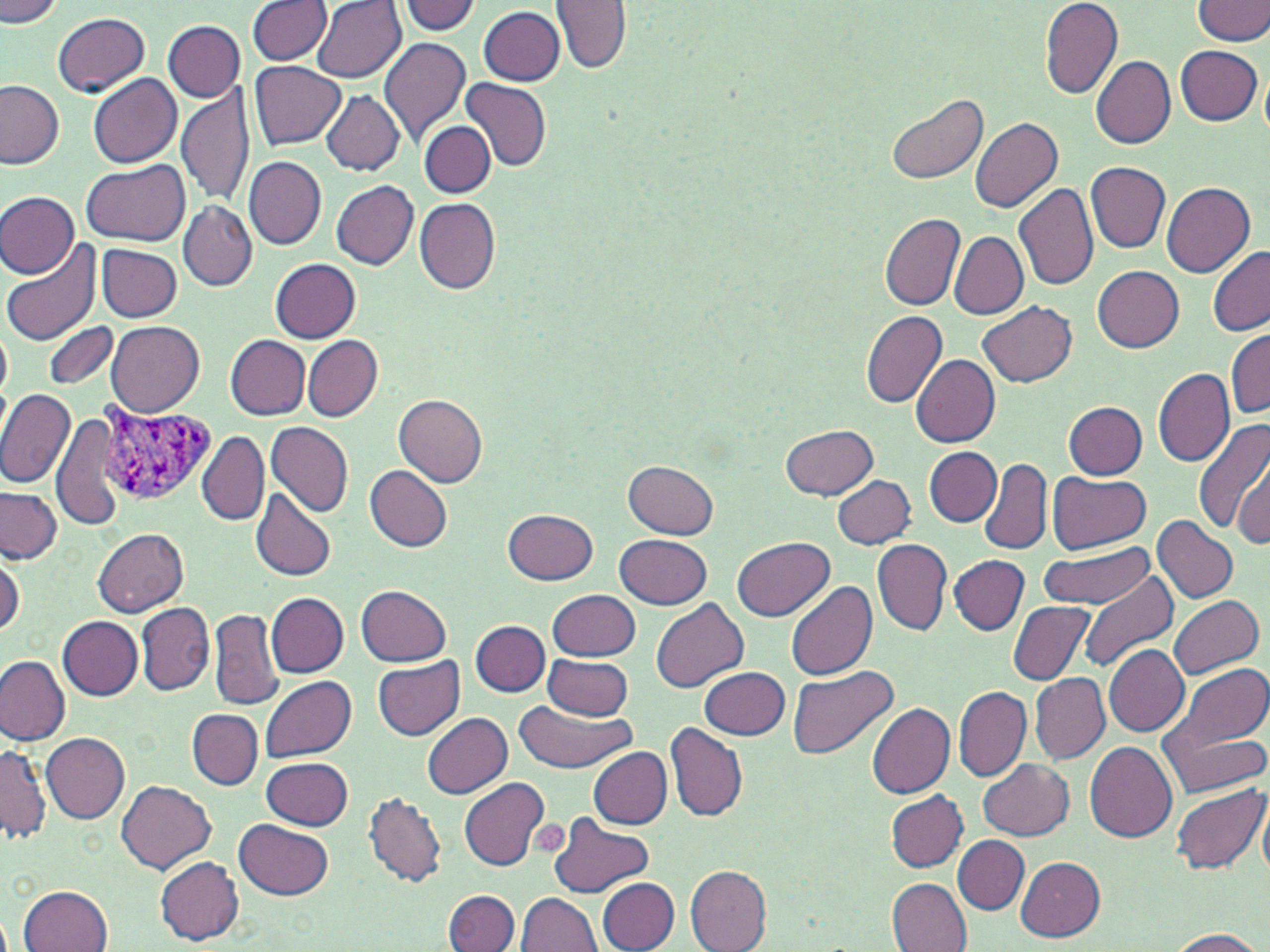
slide_level_diagnosis: Plasmodium vivax
platelet_locations: 'approximate bounding boxes as named x1/y1/x2/y2 corners in pixels: (x1=525, y1=819, x2=571, y2=854)'
preparation: thin blood film
field_of_view: one of a larger specimen
image_size: 1270×952 pixels
magnification: 1000x
modality: optical microscopy
plasmodium_vivax_infected_red_blood_cell_locations: 'approximate bounding boxes as named x1/y1/x2/y2 corners in pixels: (x1=94, y1=404, x2=216, y2=508)'
stain: May-Grünwald-Giemsa
uninfected_red_blood_cell_locations: 'approximate bounding boxes as named x1/y1/x2/y2 corners in pixels: (x1=399, y1=0, x2=482, y2=35), (x1=553, y1=0, x2=633, y2=75), (x1=1040, y1=0, x2=1123, y2=98), (x1=1194, y1=0, x2=1270, y2=45), (x1=1, y1=1, x2=65, y2=26), (x1=248, y1=1, x2=330, y2=65), (x1=313, y1=2, x2=404, y2=82), (x1=478, y1=6, x2=565, y2=85), (x1=53, y1=12, x2=150, y2=97), (x1=163, y1=20, x2=245, y2=100), (x1=379, y1=37, x2=471, y2=149), (x1=1175, y1=45, x2=1262, y2=125), (x1=1092, y1=55, x2=1176, y2=150), (x1=249, y1=61, x2=345, y2=149), (x1=88, y1=74, x2=182, y2=168), (x1=0, y1=78, x2=66, y2=168), (x1=460, y1=78, x2=552, y2=171), (x1=178, y1=83, x2=255, y2=209), (x1=321, y1=90, x2=405, y2=174), (x1=887, y1=92, x2=989, y2=186), (x1=970, y1=117, x2=1064, y2=213), (x1=419, y1=121, x2=495, y2=198), (x1=244, y1=155, x2=325, y2=249), (x1=83, y1=159, x2=191, y2=244), (x1=1086, y1=162, x2=1170, y2=253), (x1=331, y1=181, x2=418, y2=270), (x1=1012, y1=182, x2=1099, y2=291), (x1=1161, y1=182, x2=1256, y2=277), (x1=0, y1=190, x2=78, y2=278), (x1=414, y1=198, x2=502, y2=294), (x1=179, y1=202, x2=256, y2=291), (x1=879, y1=213, x2=967, y2=312), (x1=950, y1=232, x2=1028, y2=319), (x1=2, y1=241, x2=102, y2=347), (x1=97, y1=243, x2=182, y2=321), (x1=1206, y1=246, x2=1270, y2=336), (x1=272, y1=258, x2=360, y2=342), (x1=1092, y1=266, x2=1184, y2=353), (x1=978, y1=301, x2=1077, y2=387), (x1=861, y1=309, x2=947, y2=409), (x1=106, y1=319, x2=205, y2=417), (x1=1, y1=322, x2=12, y2=402), (x1=42, y1=322, x2=118, y2=390), (x1=1228, y1=328, x2=1270, y2=418), (x1=226, y1=335, x2=310, y2=418), (x1=304, y1=335, x2=382, y2=420), (x1=911, y1=355, x2=1000, y2=447), (x1=1153, y1=368, x2=1235, y2=467), (x1=0, y1=389, x2=76, y2=487), (x1=394, y1=395, x2=488, y2=487), (x1=1063, y1=401, x2=1147, y2=479), (x1=52, y1=413, x2=124, y2=531), (x1=1194, y1=417, x2=1270, y2=539), (x1=266, y1=421, x2=354, y2=517), (x1=781, y1=424, x2=878, y2=500), (x1=197, y1=431, x2=268, y2=527), (x1=1231, y1=441, x2=1270, y2=546), (x1=925, y1=448, x2=1002, y2=526), (x1=978, y1=457, x2=1053, y2=557), (x1=624, y1=460, x2=719, y2=538), (x1=364, y1=465, x2=453, y2=551), (x1=1048, y1=472, x2=1151, y2=554), (x1=833, y1=475, x2=914, y2=549), (x1=843, y1=479, x2=932, y2=605), (x1=0, y1=487, x2=62, y2=564), (x1=250, y1=488, x2=337, y2=582), (x1=503, y1=508, x2=598, y2=585), (x1=1152, y1=515, x2=1239, y2=604), (x1=92, y1=528, x2=188, y2=615), (x1=614, y1=534, x2=712, y2=607), (x1=734, y1=537, x2=833, y2=620), (x1=872, y1=539, x2=952, y2=636), (x1=1039, y1=543, x2=1156, y2=608), (x1=0, y1=549, x2=24, y2=638), (x1=949, y1=554, x2=1029, y2=635), (x1=1081, y1=572, x2=1179, y2=673), (x1=786, y1=578, x2=878, y2=681), (x1=357, y1=584, x2=453, y2=666), (x1=548, y1=588, x2=641, y2=661), (x1=266, y1=592, x2=349, y2=676), (x1=1167, y1=594, x2=1263, y2=678), (x1=651, y1=598, x2=749, y2=692), (x1=137, y1=601, x2=213, y2=696), (x1=1009, y1=601, x2=1094, y2=685), (x1=207, y1=608, x2=285, y2=710), (x1=58, y1=615, x2=144, y2=701), (x1=471, y1=620, x2=550, y2=697), (x1=1103, y1=645, x2=1190, y2=736), (x1=0, y1=655, x2=70, y2=746), (x1=543, y1=655, x2=634, y2=721), (x1=373, y1=657, x2=464, y2=740), (x1=1166, y1=662, x2=1269, y2=755), (x1=788, y1=665, x2=898, y2=761), (x1=698, y1=667, x2=790, y2=740), (x1=1029, y1=674, x2=1110, y2=763), (x1=263, y1=676, x2=357, y2=762), (x1=945, y1=685, x2=1109, y2=774), (x1=954, y1=686, x2=1031, y2=783), (x1=1156, y1=696, x2=1270, y2=799), (x1=514, y1=700, x2=634, y2=774), (x1=867, y1=702, x2=954, y2=799), (x1=188, y1=711, x2=263, y2=789), (x1=423, y1=713, x2=513, y2=798), (x1=663, y1=721, x2=748, y2=823), (x1=41, y1=731, x2=130, y2=822), (x1=0, y1=740, x2=50, y2=847), (x1=1084, y1=742, x2=1178, y2=842), (x1=589, y1=749, x2=672, y2=828), (x1=262, y1=757, x2=353, y2=831), (x1=978, y1=759, x2=1072, y2=839), (x1=460, y1=777, x2=549, y2=869), (x1=116, y1=781, x2=216, y2=875), (x1=1170, y1=783, x2=1267, y2=876), (x1=1258, y1=788, x2=1270, y2=881), (x1=363, y1=790, x2=447, y2=888), (x1=885, y1=791, x2=968, y2=871), (x1=546, y1=811, x2=655, y2=898), (x1=236, y1=820, x2=334, y2=899), (x1=953, y1=836, x2=1029, y2=913), (x1=155, y1=856, x2=244, y2=944), (x1=1015, y1=856, x2=1105, y2=941), (x1=685, y1=866, x2=772, y2=952), (x1=885, y1=877, x2=970, y2=951), (x1=598, y1=878, x2=678, y2=952), (x1=19, y1=884, x2=114, y2=952), (x1=444, y1=891, x2=519, y2=952), (x1=517, y1=891, x2=604, y2=951), (x1=1166, y1=928, x2=1266, y2=951)'